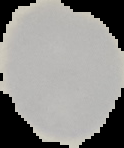
Summary:
  - Image size: 124×148 pixels
  - Image type: segmented cell region with the area outside set to black
  - Malaria status: uninfected
  - Preparation: thin blood smear